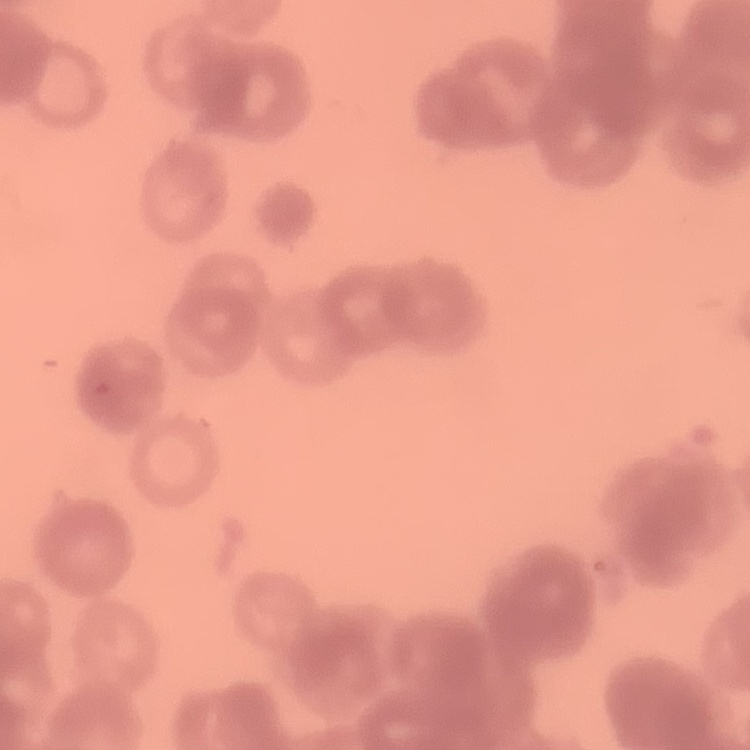
erythrocyte morphology = rouleaux formation
image type = one tile cut from a larger photomicrograph
preparation = thin peripheral smear
stain = Field's or Giemsa